Locate every Plasmodium parasite and every leukocyte.
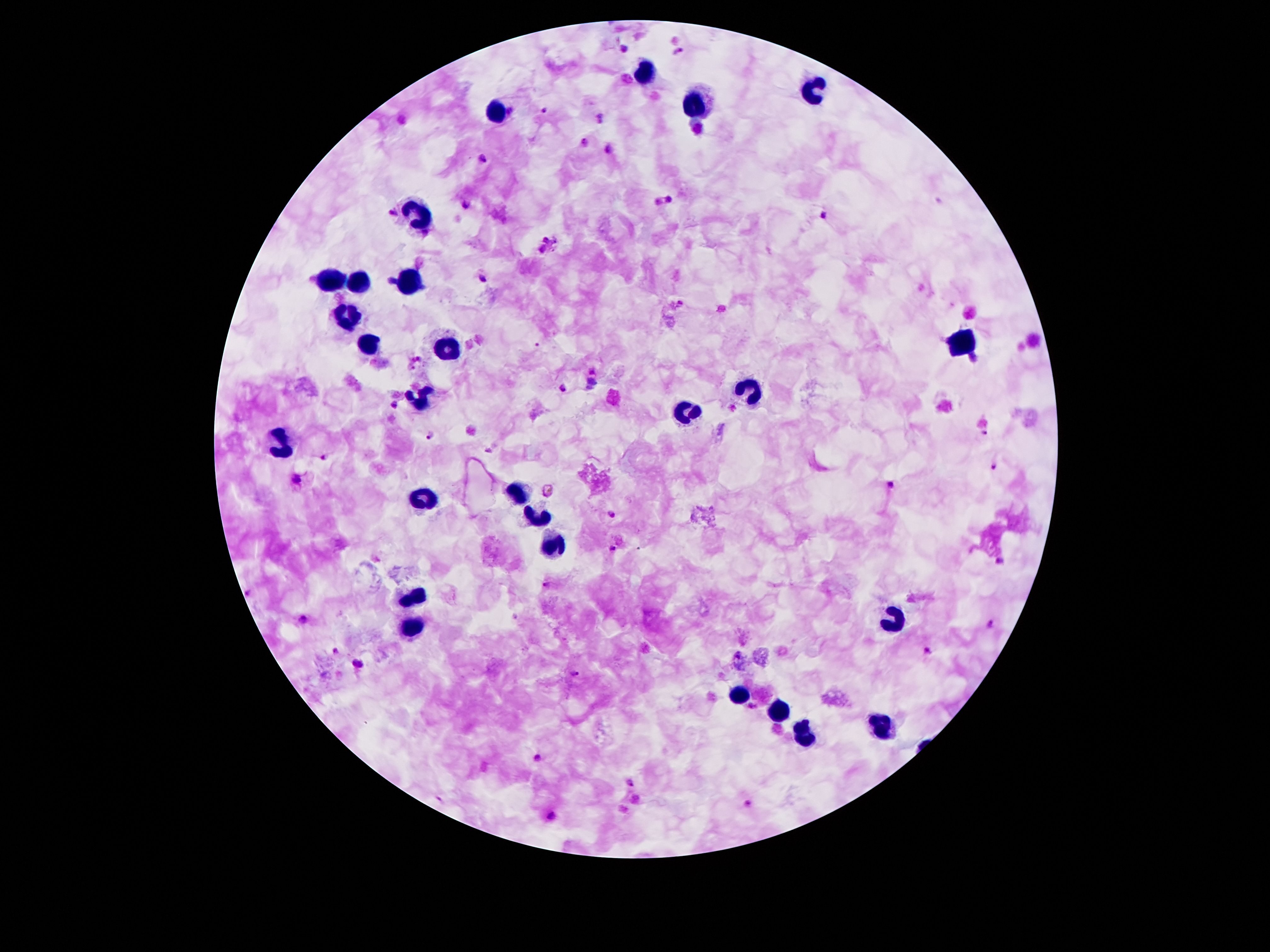
Approximate centers as {x, y} in pixels.
Plasmodium parasites: {622, 49}, {677, 51}, {544, 110}, {509, 111}, {601, 119}, {698, 130}, {583, 142}, {609, 149}, {482, 158}, {669, 200}, {466, 203}, {391, 212}, {822, 213}, {548, 243}, {484, 281}, {390, 283}, {973, 358}, {593, 372}, {592, 381}, {564, 388}, {588, 388}, {395, 403}, {986, 433}, {432, 434}, {322, 459}, {993, 467}, {296, 478}, {891, 484}, {548, 490}, {609, 516}, {612, 549}, {1000, 563}, {547, 583}, {302, 618}, {990, 624}, {928, 650}, {335, 652}, {359, 663}, {574, 671}, {752, 706}, {538, 757}, {630, 781}, {437, 800}, {750, 803}, {554, 815}.
Leukocytes: {645, 73}, {813, 88}, {693, 104}, {497, 110}, {422, 217}, {331, 281}, {357, 281}, {410, 287}, {349, 314}, {366, 345}, {961, 345}, {448, 351}, {753, 391}, {417, 402}, {687, 413}, {278, 440}, {519, 490}, {422, 497}, {534, 517}, {552, 544}, {415, 594}, {890, 621}, {413, 625}, {738, 694}, {777, 711}, {879, 725}, {802, 734}.

patient malaria status = infected with Plasmodium falciparum
capture = smartphone through the microscope eyepiece
preparation = thick blood smear
field of view = single
stain = Giemsa
image size = 1270×952 pixels
magnification = 100x